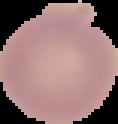

Summary:
  - Preparation: thin blood film
  - Result: no malaria parasites seen
  - Image type: segmented cell region with the area outside set to black
  - Image size: 118×124 pixels